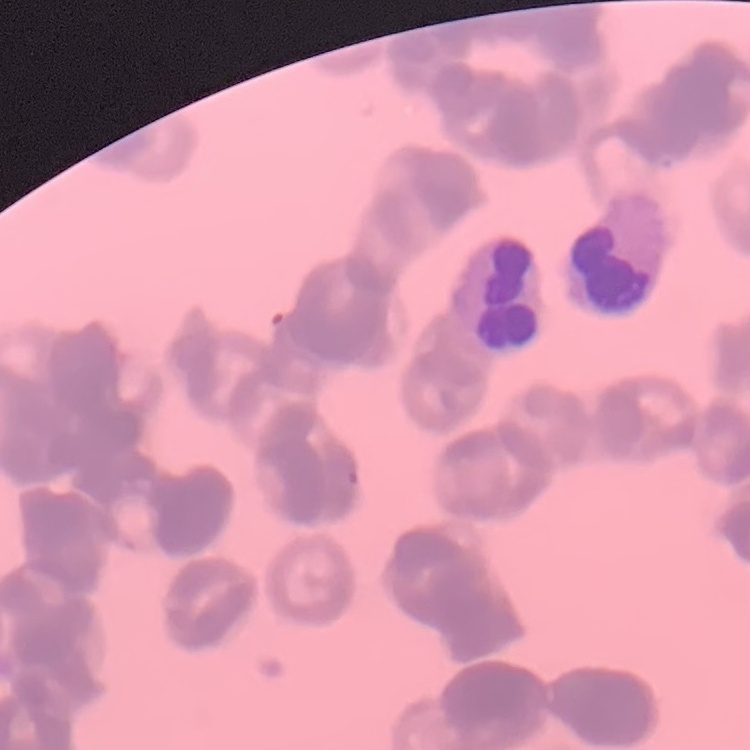
The erythrocytes exhibit rouleaux formation. Stained with either Field's or Giemsa. One tile cut from a larger photomicrograph. Thin blood smear.